Report the malaria status of this cell.
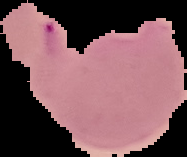

It is parasitized.

Summary:
  - Preparation: thin blood smear
  - Image type: segmented cell region on a black background
  - Image size: 187×157 pixels